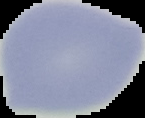
image_type: segmented cell region on a black background
preparation: thin blood film
image_size: 145×118 pixels
result: no malaria parasites detected